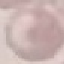
Summary:
  - Result: no malaria parasites detected
  - Stain: Giemsa
  - Capture: smartphone camera at the microscope eyepiece
  - Preparation: thin smear
  - Image type: automatically extracted cell patch, resized to 64 × 64 pixels